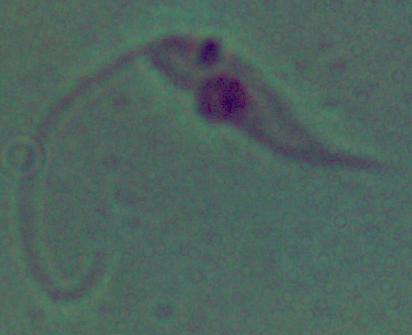 A Leishmania parasite is seen. Photomicrograph. 1000x magnification.